State which parasite is depicted.
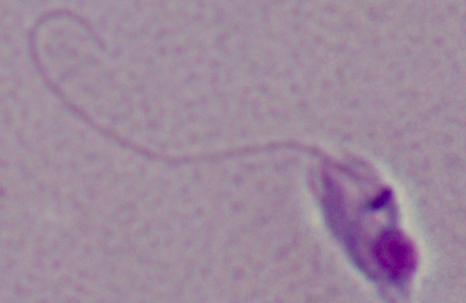
This is Leishmania.

Summary:
  - Magnification: 1000x
  - Modality: photomicrograph